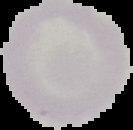
Cell region segmented out of the field of view; the surrounding area is masked to black. Result: negative for Plasmodium parasites. From a thin blood smear. Image is 133×130 pixels.